Point out each Plasmodium parasite.
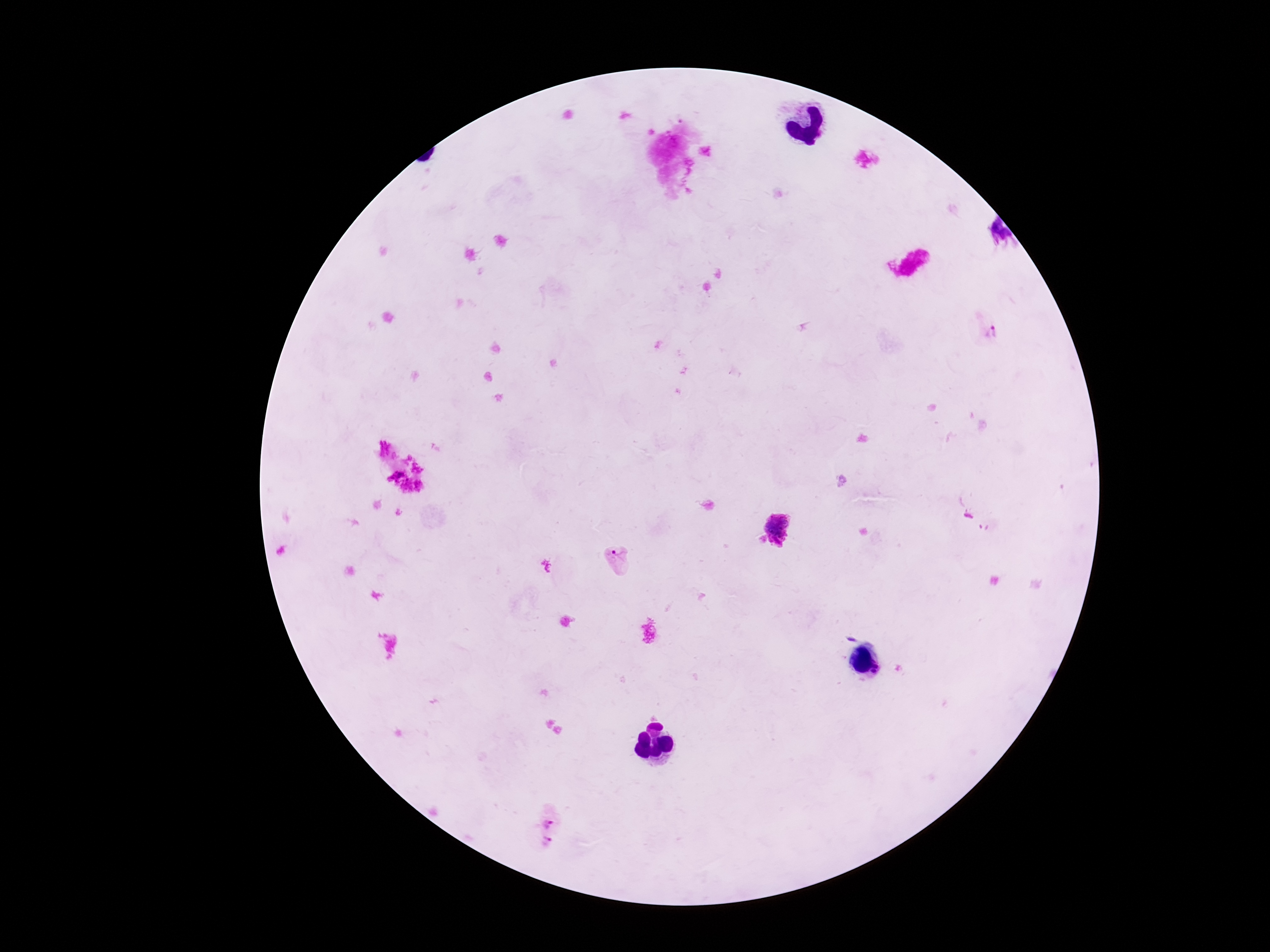

Approximate centers as [x, y] in pixels.
Plasmodium parasites: [991, 332], [777, 529], [617, 561], [549, 819], [545, 844].

{
  "stain": "Giemsa",
  "preparation": "thick blood film",
  "image_size": "1270×952 pixels",
  "field_of_view": "one from this slide",
  "patient_malaria_status": "infected",
  "capture": "smartphone camera through the microscope eyepiece",
  "magnification": "100x"
}